Report the malaria status of this cell.
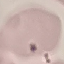
It is uninfected.

Giemsa stain. Thin smear of blood. Automatically extracted cell patch, resized to 64 × 64 pixels. Photographed with a smartphone camera at the microscope eyepiece.